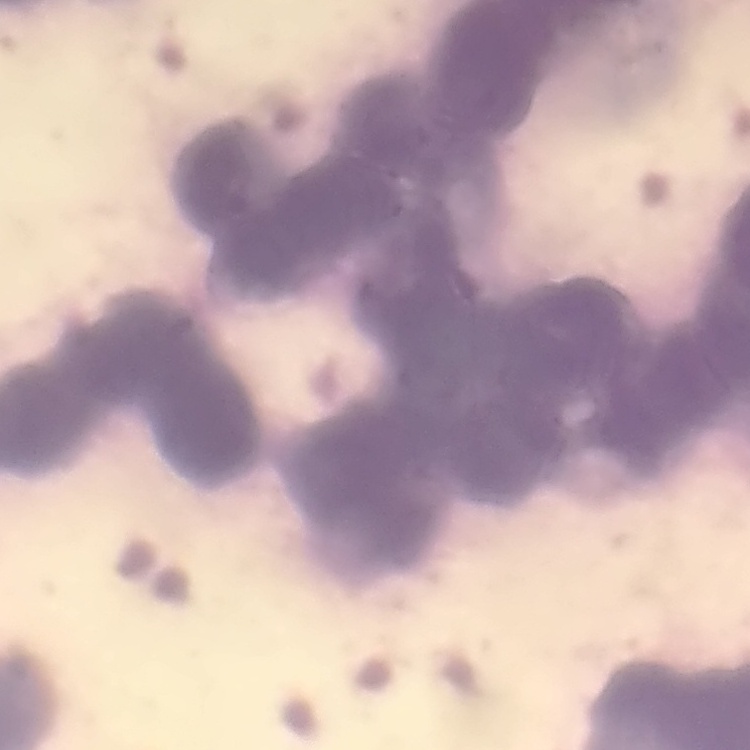 The red blood cells show rouleaux formation. Field's or Giemsa stain. One tile cut from a larger photomicrograph. Thin blood smear.